Evaluate for malaria.
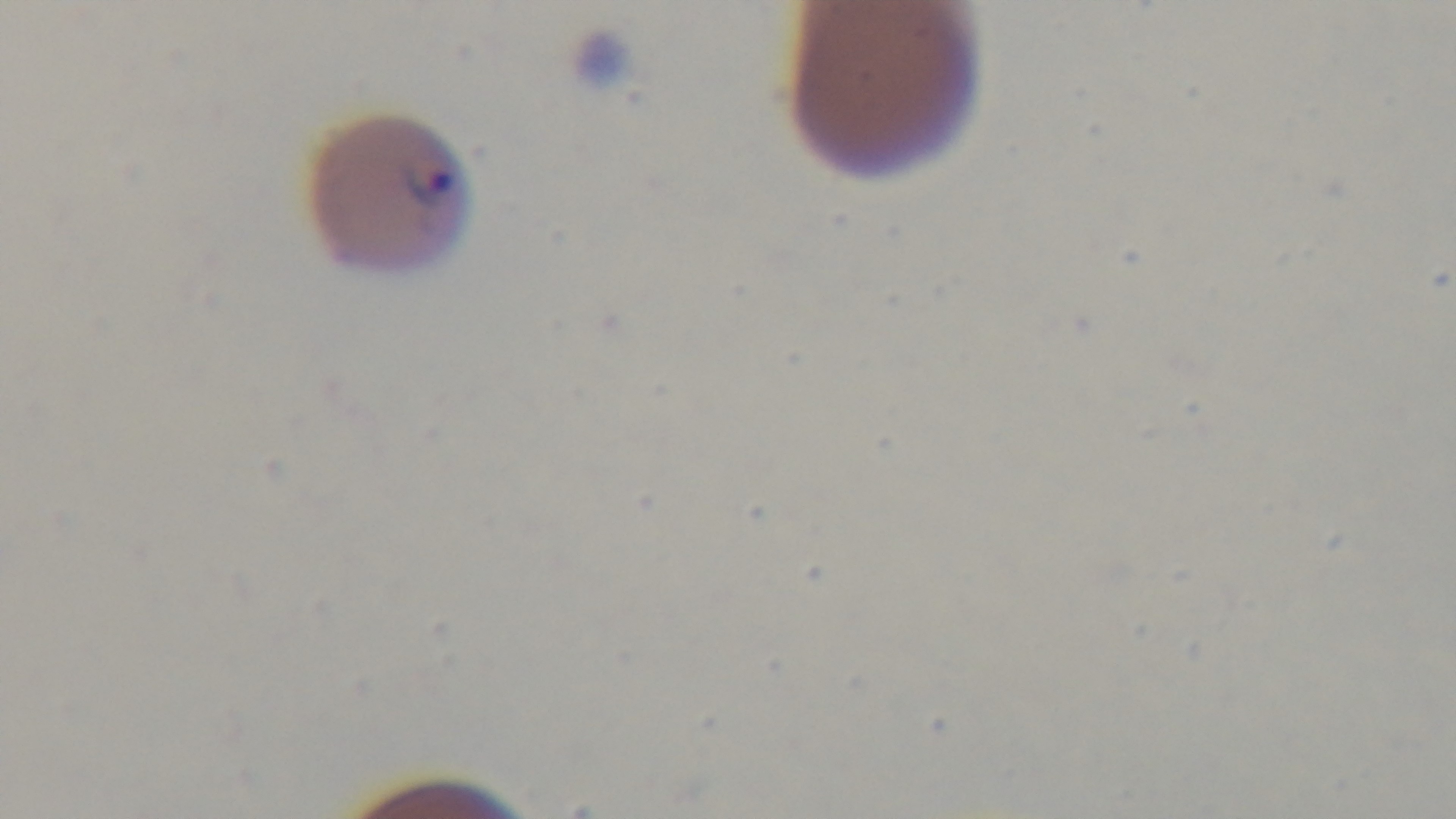

Infected.

Oil-immersion objective, 100x. Giemsa stain. Captured with a mounted 4K digital camera. Preparation: thin blood film. Photomicrograph. Single field of view.